Outline each blood parasite and name the species.
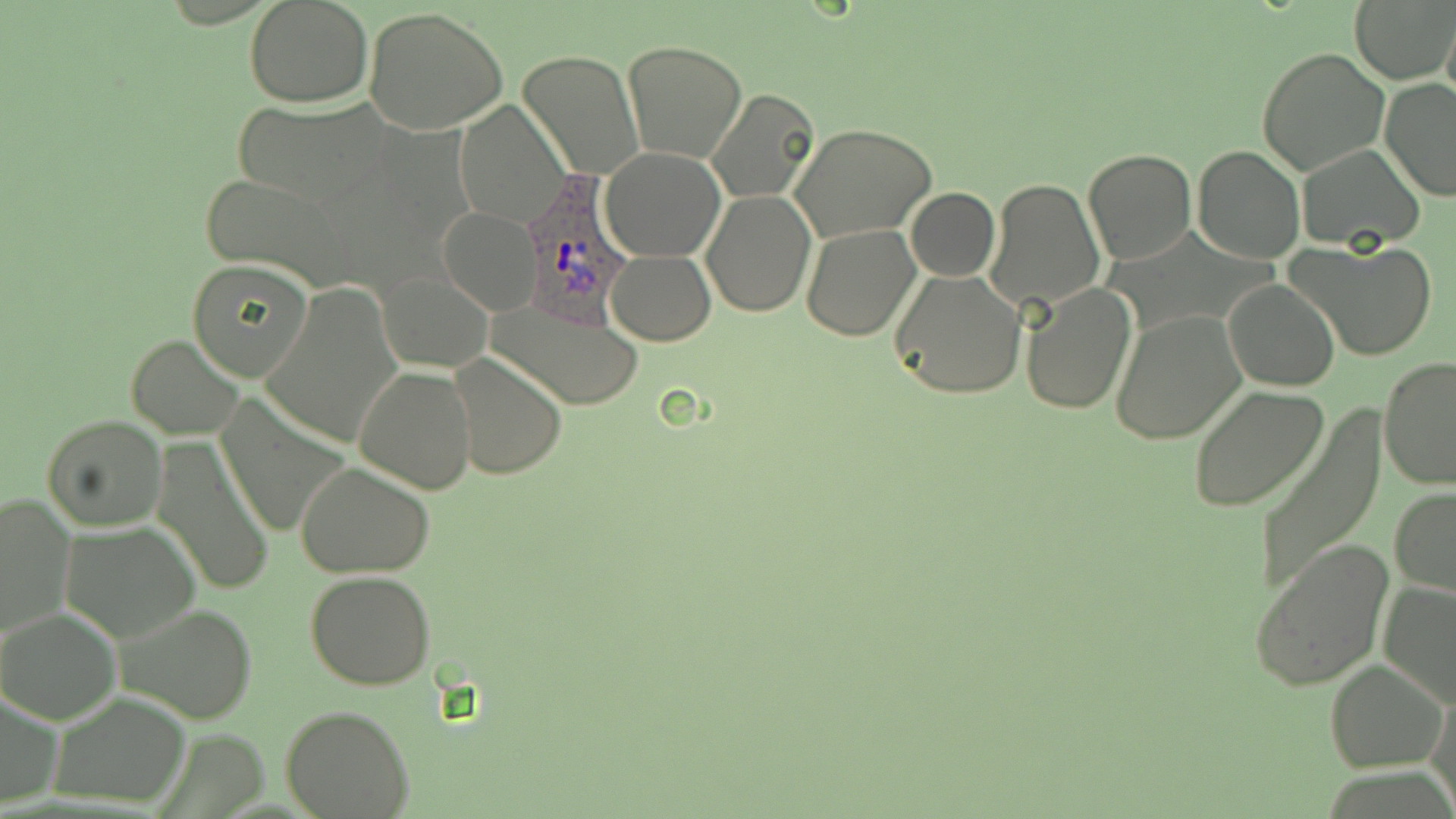

Approximate bounding boxes as named x1/y1/x2/y2 corners in pixels.
Plasmodium ovale-infected red blood cells: (x1=520, y1=182, x2=632, y2=323).
No Plasmodium falciparum, Plasmodium malariae, Plasmodium vivax, Babesia divergens, or Trypanosoma brucei observed.

slide_level_diagnosis: Plasmodium ovale
field_of_view: one of a larger specimen
preparation: thin blood film
uninfected_red_blood_cell_locations: 'approximate bounding boxes as named x1/y1/x2/y2 corners in pixels: (x1=245, y1=0, x2=373, y2=106), (x1=1350, y1=0, x2=1456, y2=85), (x1=364, y1=7, x2=510, y2=136), (x1=1442, y1=12, x2=1456, y2=110), (x1=622, y1=40, x2=747, y2=164), (x1=1257, y1=47, x2=1389, y2=177), (x1=518, y1=51, x2=643, y2=180), (x1=1379, y1=79, x2=1456, y2=202), (x1=704, y1=87, x2=822, y2=204), (x1=233, y1=99, x2=392, y2=208), (x1=455, y1=102, x2=568, y2=229), (x1=791, y1=123, x2=936, y2=243), (x1=1295, y1=143, x2=1426, y2=251), (x1=1191, y1=144, x2=1304, y2=263), (x1=601, y1=146, x2=725, y2=261), (x1=1082, y1=146, x2=1197, y2=265), (x1=197, y1=174, x2=355, y2=287), (x1=983, y1=177, x2=1106, y2=313), (x1=905, y1=187, x2=1000, y2=282), (x1=701, y1=191, x2=815, y2=317), (x1=438, y1=209, x2=541, y2=314), (x1=800, y1=224, x2=920, y2=341), (x1=1287, y1=238, x2=1437, y2=363), (x1=606, y1=249, x2=716, y2=345), (x1=186, y1=260, x2=314, y2=382), (x1=887, y1=266, x2=1027, y2=400), (x1=378, y1=271, x2=493, y2=372), (x1=1224, y1=278, x2=1340, y2=391), (x1=265, y1=281, x2=403, y2=450), (x1=1021, y1=285, x2=1137, y2=414), (x1=489, y1=296, x2=642, y2=410), (x1=1110, y1=311, x2=1246, y2=444), (x1=127, y1=334, x2=243, y2=440), (x1=448, y1=352, x2=567, y2=479), (x1=1378, y1=356, x2=1456, y2=489), (x1=354, y1=364, x2=477, y2=495), (x1=1187, y1=386, x2=1330, y2=512), (x1=215, y1=395, x2=350, y2=542), (x1=1252, y1=409, x2=1389, y2=595), (x1=41, y1=416, x2=166, y2=531), (x1=151, y1=438, x2=276, y2=598), (x1=294, y1=461, x2=436, y2=577), (x1=1389, y1=487, x2=1456, y2=596), (x1=1, y1=492, x2=75, y2=639), (x1=61, y1=522, x2=202, y2=644), (x1=1247, y1=539, x2=1395, y2=692), (x1=305, y1=571, x2=437, y2=692), (x1=1379, y1=579, x2=1456, y2=710), (x1=116, y1=603, x2=257, y2=725), (x1=1, y1=609, x2=121, y2=724), (x1=1324, y1=658, x2=1449, y2=771), (x1=1428, y1=683, x2=1456, y2=812), (x1=0, y1=689, x2=64, y2=811), (x1=49, y1=692, x2=191, y2=807), (x1=282, y1=706, x2=414, y2=819)'
stain: May-Grünwald-Giemsa
image_size: 1456×819 pixels
magnification: 1000x
modality: light microscopy